Locate every blood parasite and identify its species.
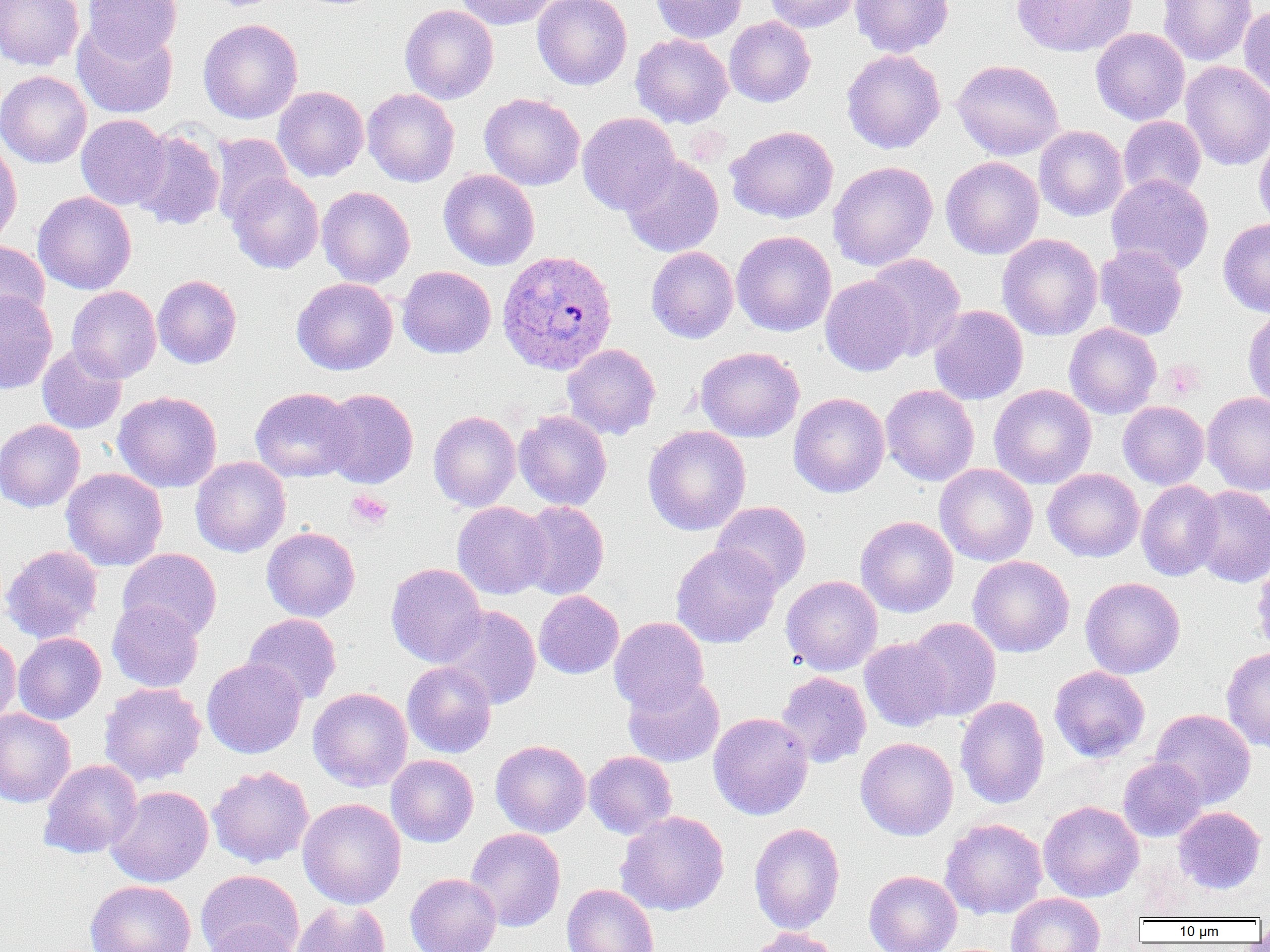

Approximate bounding boxes as [x1, y1, x2, y2] in pixels.
Plasmodium ovale-infected red blood cells: [497, 249, 619, 375].
No Plasmodium falciparum, Plasmodium malariae, Plasmodium vivax, Babesia divergens, or Trypanosoma brucei observed.

slide-level diagnosis = Plasmodium ovale
uninfected red blood cell locations = approximate bounding boxes as [x1, y1, x2, y2] in pixels: [0, 0, 84, 70], [83, 0, 182, 61], [453, 0, 560, 30], [533, 0, 633, 90], [651, 0, 746, 43], [763, 0, 863, 33], [851, 0, 954, 58], [1011, 0, 1136, 57], [1157, 0, 1258, 66], [399, 4, 499, 104], [1238, 4, 1270, 104], [724, 17, 816, 107], [198, 19, 303, 124], [72, 21, 178, 119], [1090, 27, 1190, 125], [630, 33, 733, 128], [841, 49, 946, 154], [952, 59, 1064, 161], [1180, 61, 1270, 171], [0, 70, 91, 168], [273, 86, 369, 182], [362, 88, 460, 187], [480, 93, 585, 190], [577, 111, 680, 215], [76, 114, 170, 210], [1118, 116, 1206, 199], [726, 125, 838, 223], [1034, 126, 1129, 221], [130, 129, 225, 231], [1254, 130, 1270, 231], [210, 133, 295, 225], [0, 137, 23, 250], [621, 155, 724, 257], [941, 156, 1044, 259], [827, 161, 938, 271], [439, 169, 540, 270], [226, 172, 324, 274], [1106, 173, 1214, 276], [317, 186, 415, 288], [33, 191, 136, 294], [1218, 218, 1270, 317], [731, 230, 837, 336], [997, 233, 1103, 340], [0, 240, 50, 326], [1094, 244, 1188, 340], [646, 246, 739, 343], [862, 253, 966, 360], [397, 266, 496, 359], [153, 274, 242, 368], [820, 274, 917, 377], [291, 277, 398, 375], [66, 285, 161, 383], [0, 290, 58, 394], [929, 305, 1028, 405], [1242, 308, 1270, 409], [1063, 322, 1162, 419], [562, 343, 661, 440], [37, 344, 127, 434], [694, 346, 805, 442], [880, 384, 980, 486], [989, 384, 1096, 489], [250, 387, 356, 482], [319, 388, 419, 488], [113, 391, 222, 493], [1202, 391, 1270, 495], [788, 392, 890, 497], [1118, 401, 1209, 489], [428, 410, 521, 512], [514, 410, 612, 510], [0, 419, 85, 512], [642, 425, 751, 535], [190, 456, 291, 557], [935, 463, 1038, 566], [61, 468, 168, 571], [1043, 468, 1144, 562], [1136, 480, 1224, 581], [1190, 485, 1270, 587], [516, 500, 610, 600], [711, 501, 811, 595], [452, 502, 552, 600], [855, 515, 958, 617], [261, 526, 360, 622], [670, 543, 781, 648], [1, 544, 103, 643], [117, 548, 221, 641], [1251, 554, 1270, 657], [967, 555, 1075, 657], [386, 563, 487, 668], [781, 575, 883, 676], [1080, 577, 1185, 679], [534, 590, 624, 679], [107, 600, 204, 693], [437, 605, 541, 709], [242, 613, 342, 705], [609, 616, 709, 713], [904, 617, 1001, 721], [0, 632, 20, 729], [13, 632, 106, 724], [859, 637, 953, 731], [1221, 646, 1270, 753], [202, 657, 308, 759], [401, 661, 497, 758], [1049, 665, 1150, 763], [775, 672, 872, 768], [622, 674, 725, 768], [100, 682, 206, 786], [308, 687, 413, 791], [955, 696, 1050, 809], [0, 708, 76, 808], [1150, 708, 1256, 808], [708, 712, 813, 820], [855, 737, 958, 840], [490, 739, 591, 838], [584, 750, 678, 839], [386, 755, 479, 847], [1117, 756, 1207, 842], [38, 759, 143, 859], [207, 765, 314, 868], [106, 786, 213, 887], [298, 798, 406, 909], [1038, 801, 1144, 902], [1173, 806, 1266, 894], [615, 811, 729, 916], [940, 818, 1048, 919], [749, 822, 845, 934], [465, 827, 566, 932], [196, 869, 304, 952], [864, 870, 962, 952], [405, 873, 502, 952], [85, 880, 196, 952], [562, 883, 659, 952], [1005, 893, 1105, 952], [292, 899, 391, 952], [201, 921, 304, 952], [744, 927, 844, 952]
modality = light microscopy
field of view = one of a larger specimen
platelet locations = approximate bounding boxes as [x1, y1, x2, y2] in pixels: [1161, 361, 1204, 399], [347, 489, 393, 528]
image size = 1270×952 pixels
magnification = 1000x
preparation = thin blood film